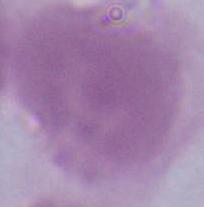

Summary:
  - Identification: erythrocyte
  - Magnification: 1000x
  - Modality: micrograph